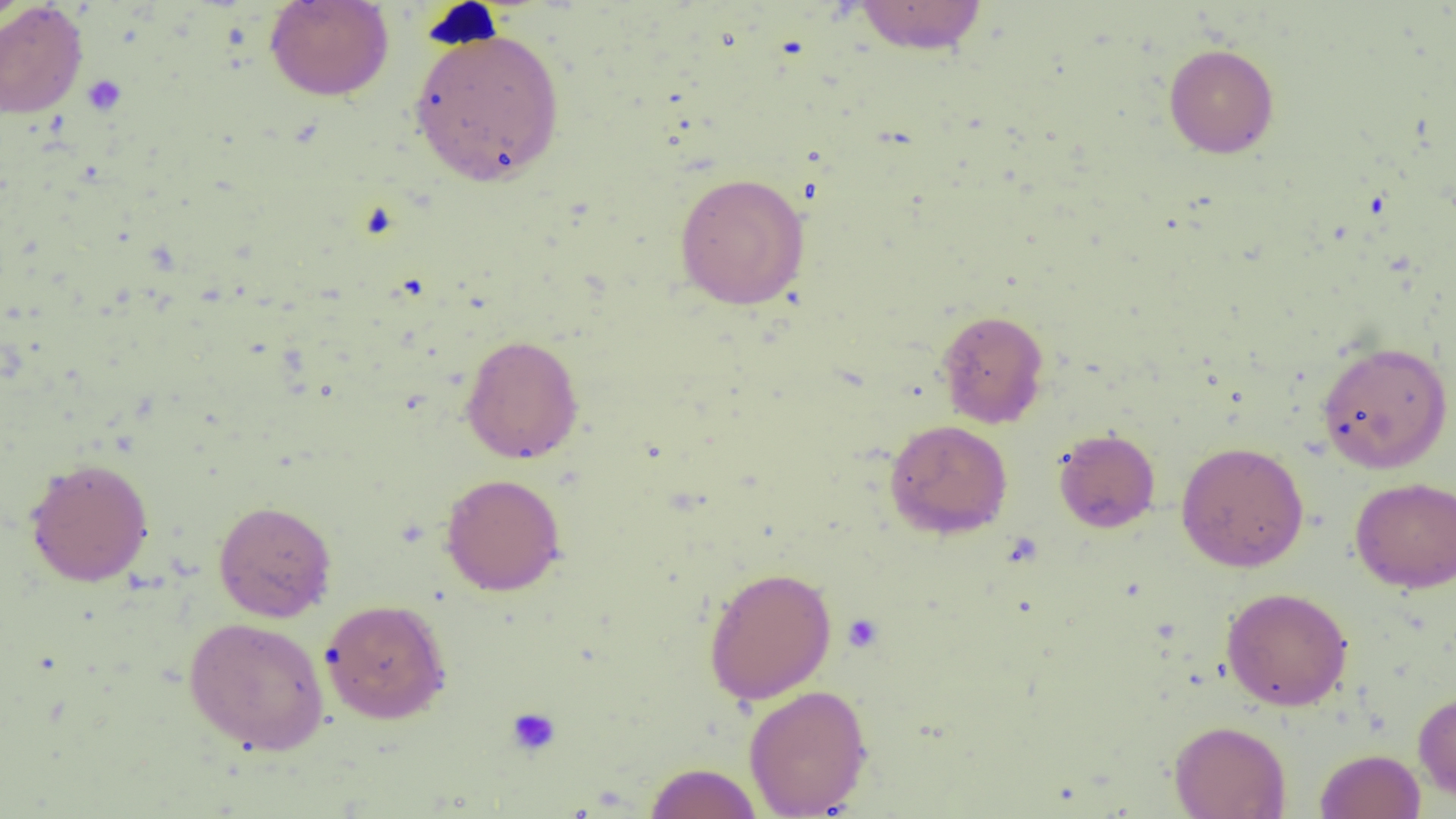
Summary:
  - Coordinate format: approximate bounding boxes as (x1, y1, x2, y2) in pixels
  - Platelet locations: (420, 2, 503, 51), (81, 75, 127, 116), (842, 613, 884, 653), (505, 707, 561, 757)
  - Uninfected red blood cell locations: (264, 0, 394, 101), (853, 0, 989, 56), (0, 1, 32, 31), (0, 2, 88, 119), (409, 26, 565, 185), (1163, 43, 1279, 158), (674, 171, 811, 310), (937, 309, 1050, 428), (460, 333, 584, 464), (1316, 341, 1454, 474), (884, 419, 1012, 539), (1053, 428, 1160, 533), (1175, 441, 1309, 572), (24, 457, 154, 586), (440, 473, 566, 596), (1350, 477, 1456, 592), (213, 500, 337, 622), (703, 566, 837, 704), (1221, 587, 1353, 711), (320, 598, 451, 724), (184, 616, 329, 755), (744, 684, 873, 818), (1413, 690, 1456, 803), (1169, 719, 1291, 819), (1315, 748, 1425, 819), (644, 762, 763, 819)
  - Slide-level diagnosis: negative for blood parasites
  - Image size: 1456×819 pixels
  - Field of view: one of a larger specimen
  - Magnification: 1000x
  - Modality: light microscopy
  - Preparation: thin blood smear